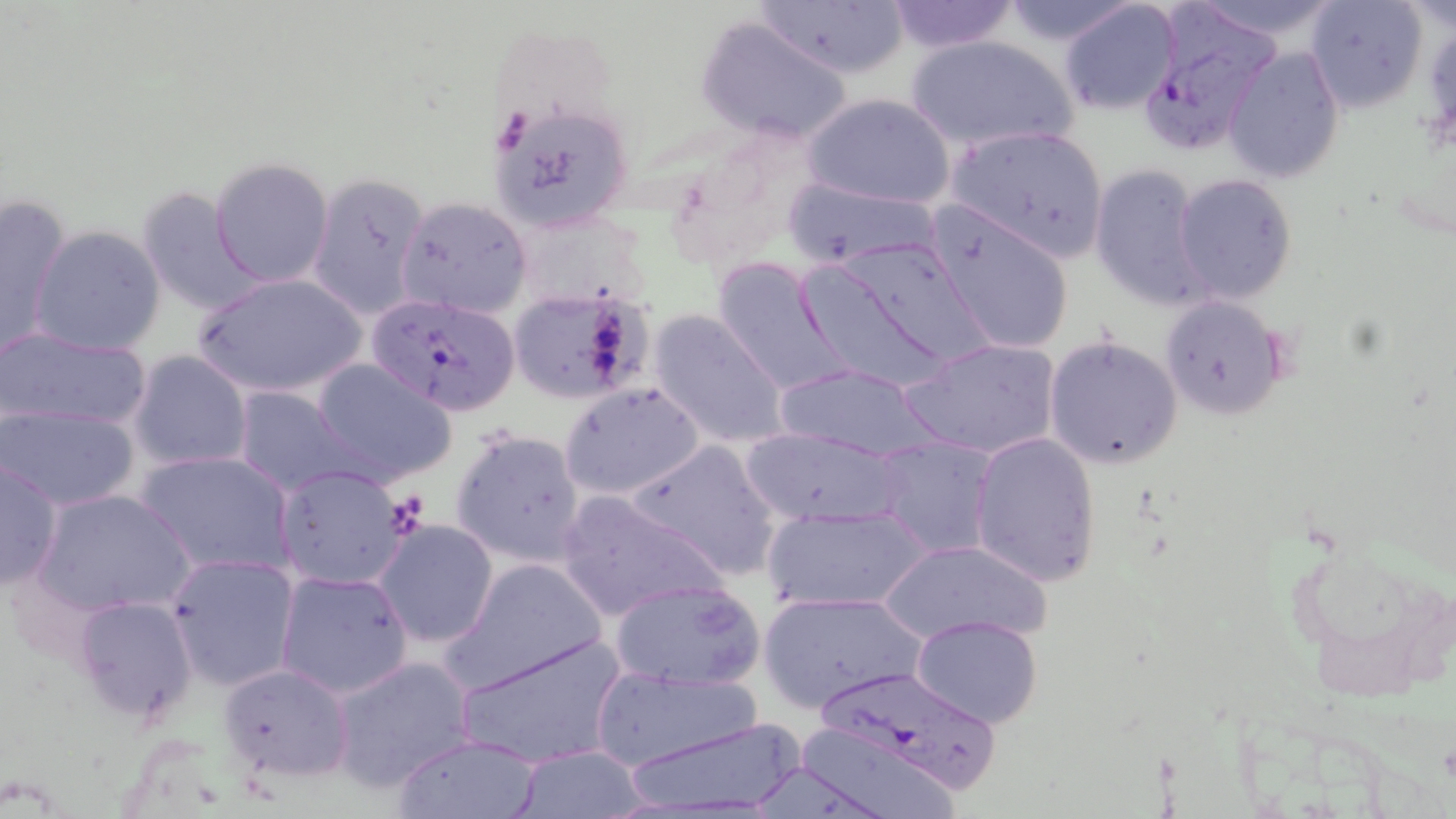

Approximate bounding boxes as named x1/y1/x2/y2 corners in pixels. Uninfected red blood cell locations: (x1=753, y1=0, x2=911, y2=82), (x1=885, y1=0, x2=1020, y2=53), (x1=997, y1=0, x2=1141, y2=45), (x1=1304, y1=0, x2=1429, y2=114), (x1=1057, y1=1, x2=1185, y2=116), (x1=695, y1=15, x2=854, y2=147), (x1=902, y1=34, x2=1080, y2=153), (x1=1224, y1=45, x2=1344, y2=184), (x1=802, y1=91, x2=956, y2=210), (x1=490, y1=102, x2=635, y2=233), (x1=944, y1=123, x2=1111, y2=264), (x1=210, y1=157, x2=335, y2=288), (x1=1090, y1=163, x2=1210, y2=311), (x1=306, y1=171, x2=430, y2=321), (x1=1173, y1=173, x2=1298, y2=305), (x1=782, y1=175, x2=943, y2=270), (x1=135, y1=187, x2=261, y2=316), (x1=396, y1=196, x2=531, y2=319), (x1=0, y1=197, x2=73, y2=353), (x1=927, y1=205, x2=1075, y2=356), (x1=28, y1=225, x2=165, y2=355), (x1=794, y1=255, x2=961, y2=393), (x1=711, y1=257, x2=854, y2=397), (x1=191, y1=273, x2=369, y2=400), (x1=506, y1=285, x2=655, y2=406), (x1=1157, y1=294, x2=1289, y2=419), (x1=649, y1=308, x2=791, y2=451), (x1=0, y1=326, x2=155, y2=437), (x1=1043, y1=331, x2=1185, y2=470), (x1=899, y1=336, x2=1064, y2=461), (x1=127, y1=350, x2=254, y2=472), (x1=312, y1=359, x2=459, y2=488), (x1=773, y1=363, x2=937, y2=460), (x1=560, y1=382, x2=706, y2=501), (x1=233, y1=386, x2=364, y2=495), (x1=1, y1=404, x2=141, y2=511), (x1=449, y1=427, x2=588, y2=567), (x1=741, y1=428, x2=908, y2=527), (x1=970, y1=431, x2=1100, y2=589), (x1=873, y1=435, x2=997, y2=560), (x1=626, y1=438, x2=785, y2=581), (x1=134, y1=450, x2=297, y2=575), (x1=0, y1=457, x2=64, y2=594), (x1=275, y1=464, x2=412, y2=590), (x1=34, y1=487, x2=196, y2=617), (x1=555, y1=489, x2=728, y2=624), (x1=761, y1=503, x2=934, y2=614), (x1=372, y1=518, x2=499, y2=648), (x1=1288, y1=532, x2=1453, y2=699), (x1=875, y1=538, x2=1051, y2=648), (x1=165, y1=553, x2=300, y2=691), (x1=443, y1=558, x2=610, y2=693), (x1=275, y1=568, x2=416, y2=699), (x1=608, y1=577, x2=767, y2=690), (x1=759, y1=589, x2=926, y2=712), (x1=75, y1=595, x2=198, y2=722), (x1=911, y1=615, x2=1043, y2=728), (x1=455, y1=633, x2=627, y2=770), (x1=330, y1=653, x2=476, y2=793), (x1=217, y1=662, x2=354, y2=783), (x1=591, y1=666, x2=765, y2=771), (x1=615, y1=715, x2=809, y2=818), (x1=796, y1=727, x2=960, y2=819), (x1=395, y1=733, x2=542, y2=819), (x1=511, y1=746, x2=651, y2=818). Plasmodium falciparum-infected red blood cell locations: (x1=1133, y1=8, x2=1282, y2=156), (x1=357, y1=295, x2=513, y2=418), (x1=807, y1=667, x2=1004, y2=792). Slide-level diagnosis: Plasmodium falciparum. May-Grünwald-Giemsa-stained preparation. Thin blood film. Single field of view. Image is 1456×819 pixels. Light microscopy. Captured at 1000x magnification.